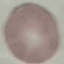
{
  "result": "no malaria parasites detected",
  "stain": "Giemsa",
  "preparation": "thin blood smear",
  "image_type": "automatically extracted cell patch, resized to 64 × 64 pixels",
  "capture": "smartphone through the microscope eyepiece"
}